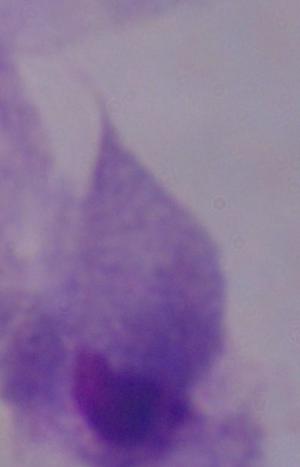
Summary:
  - Modality: photomicrograph
  - Magnification: 1000x
  - Identification: trichomonad